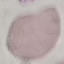
malaria status = uninfected
preparation = thin blood smear
stain = Giemsa
capture = smartphone through the microscope eyepiece
image type = automatically extracted cell patch, resized to 64 × 64 pixels